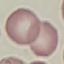

result = no malaria parasites seen
image type = automatically extracted cell patch, resized to 64 × 64 pixels
stain = Giemsa
capture = smartphone camera at the microscope eyepiece
preparation = thin blood smear